Describe the morphology of the red blood cells.
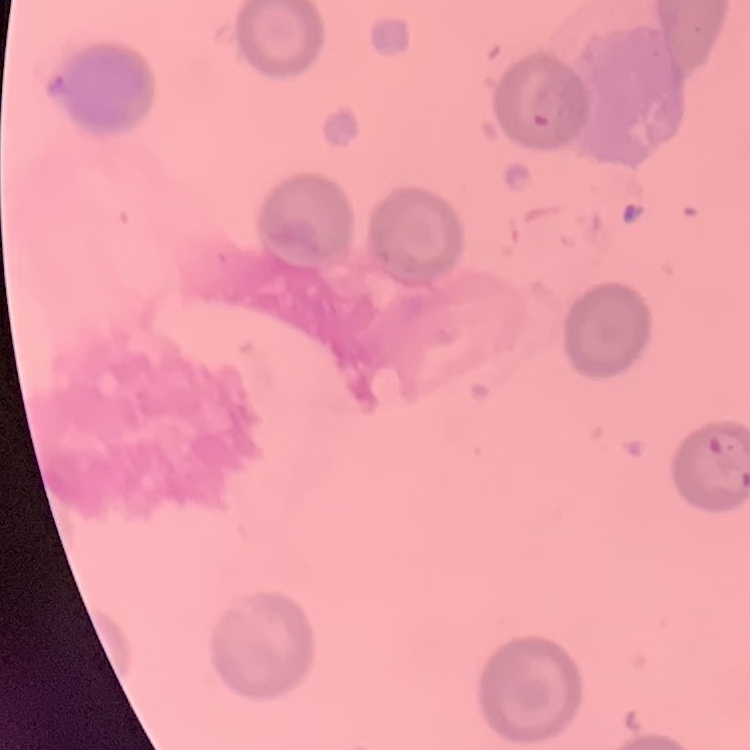

No rouleaux formation.

stain: Field's or Giemsa
preparation: thin blood smear
image_type: square crop of a larger photomicrograph